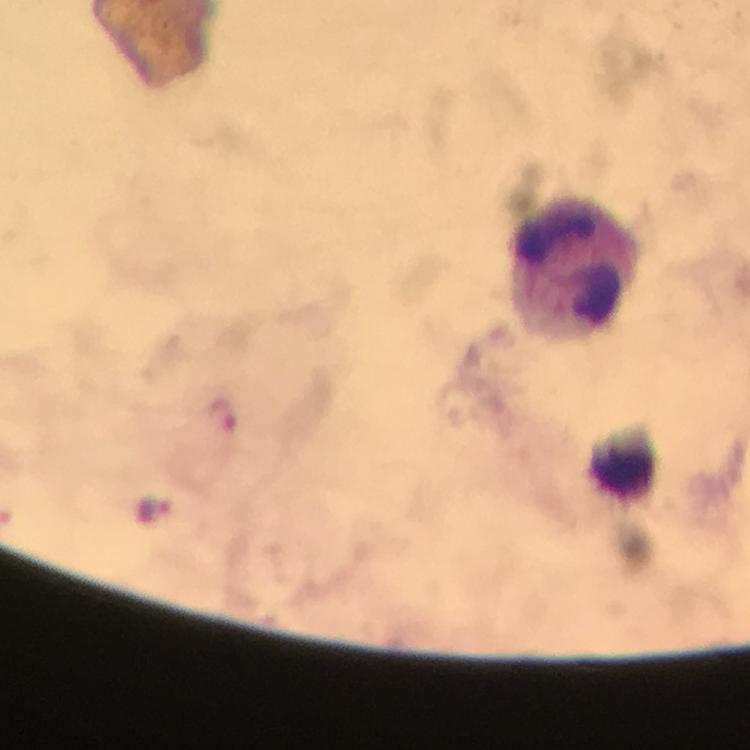

Approximate centers as [x, y] in pixels.
Summary:
  - Leukocyte locations: [573, 265], [623, 459]
  - Malaria parasite locations: [222, 416], [156, 510]
  - Image size: 750×750 pixels
  - Preparation: thick blood smear
  - Cropped from: one field of view
  - Stain: Giemsa
  - Context: from a malaria diagnostic workup
  - Magnification: 100x
  - Immersion oil: applied
  - Capture: smartphone camera through the microscope